Name the blood parasite species.
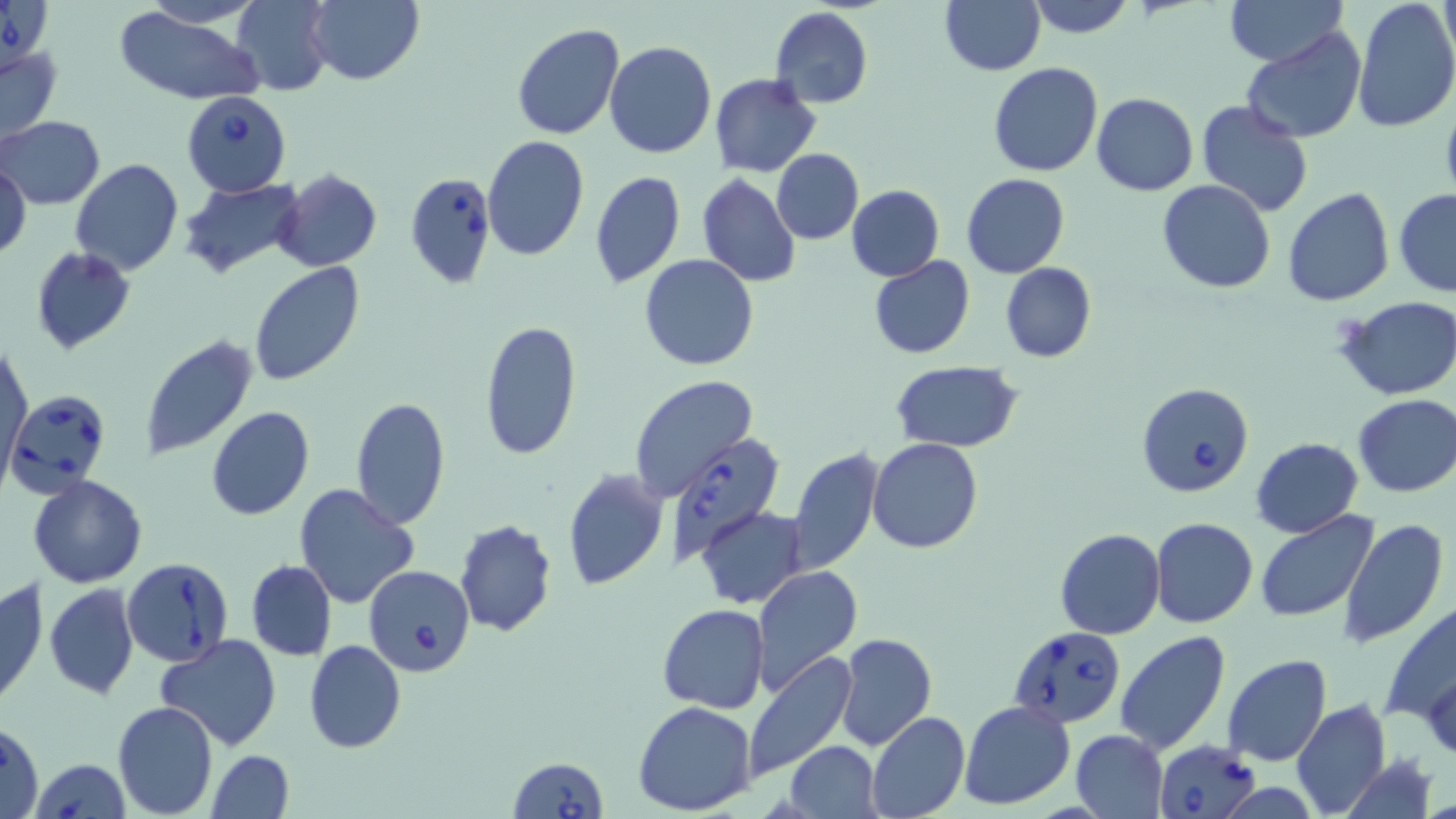
Babesia divergens.

Approximate bounding boxes as (x1, y1, x2, y2) in pixels. Babesia divergens-infected red blood cell locations: (1, 0, 48, 73), (180, 90, 292, 196), (405, 173, 495, 289), (1136, 383, 1255, 499), (7, 388, 111, 497), (659, 433, 786, 566), (121, 558, 235, 667), (363, 563, 475, 680), (1006, 627, 1126, 728), (1153, 738, 1265, 819), (508, 756, 608, 819), (31, 759, 130, 819). Uninfected red blood cell locations: (141, 0, 262, 27), (308, 0, 424, 86), (940, 0, 1045, 74), (1024, 0, 1137, 38), (1225, 0, 1346, 67), (1352, 0, 1456, 133), (1437, 0, 1455, 65), (232, 1, 335, 94), (770, 7, 873, 108), (112, 8, 264, 105), (511, 23, 625, 141), (1240, 28, 1367, 145), (604, 40, 717, 159), (0, 44, 64, 142), (989, 63, 1104, 178), (710, 73, 821, 177), (1091, 92, 1198, 195), (1195, 99, 1313, 216), (1181, 102, 1333, 300), (1, 115, 104, 210), (481, 136, 589, 260), (771, 149, 863, 244), (2, 158, 31, 260), (69, 159, 183, 275), (274, 169, 382, 272), (589, 170, 685, 289), (697, 173, 801, 288), (962, 173, 1069, 277), (176, 177, 305, 277), (663, 178, 781, 334), (1158, 179, 1275, 293), (846, 185, 944, 281), (1282, 187, 1396, 307), (1395, 188, 1456, 298), (29, 247, 137, 354), (640, 253, 760, 371), (868, 255, 975, 359), (1000, 262, 1097, 363), (248, 263, 365, 387), (1339, 296, 1456, 400), (478, 320, 583, 462), (138, 334, 259, 462), (3, 342, 33, 483), (889, 361, 1026, 451), (630, 376, 759, 503), (1352, 394, 1456, 497), (349, 395, 452, 530), (206, 406, 315, 521), (1251, 437, 1362, 538), (868, 438, 983, 553), (788, 447, 883, 577), (561, 468, 668, 590), (39, 471, 151, 705), (28, 474, 147, 587), (293, 484, 420, 609), (698, 507, 808, 609), (1254, 511, 1378, 622), (1150, 516, 1258, 626), (454, 520, 558, 637), (1338, 520, 1448, 645), (1053, 529, 1164, 641), (246, 560, 336, 660), (751, 564, 862, 693), (0, 575, 49, 712), (44, 582, 140, 700), (1380, 597, 1456, 725), (657, 603, 771, 713), (1115, 631, 1231, 755), (834, 634, 937, 752), (155, 635, 283, 752), (304, 640, 405, 754), (743, 652, 856, 783), (1223, 655, 1331, 767), (1422, 664, 1456, 763), (1290, 698, 1392, 818), (112, 700, 220, 819), (960, 700, 1076, 811), (632, 701, 757, 816), (866, 711, 969, 819), (1, 721, 44, 819), (1069, 729, 1168, 818), (785, 741, 882, 819), (209, 750, 293, 818). Single field of view. Thin blood smear. 1000x magnification. Optical microscopy. May-Grünwald-Giemsa stain. Image is 1456×819 pixels.